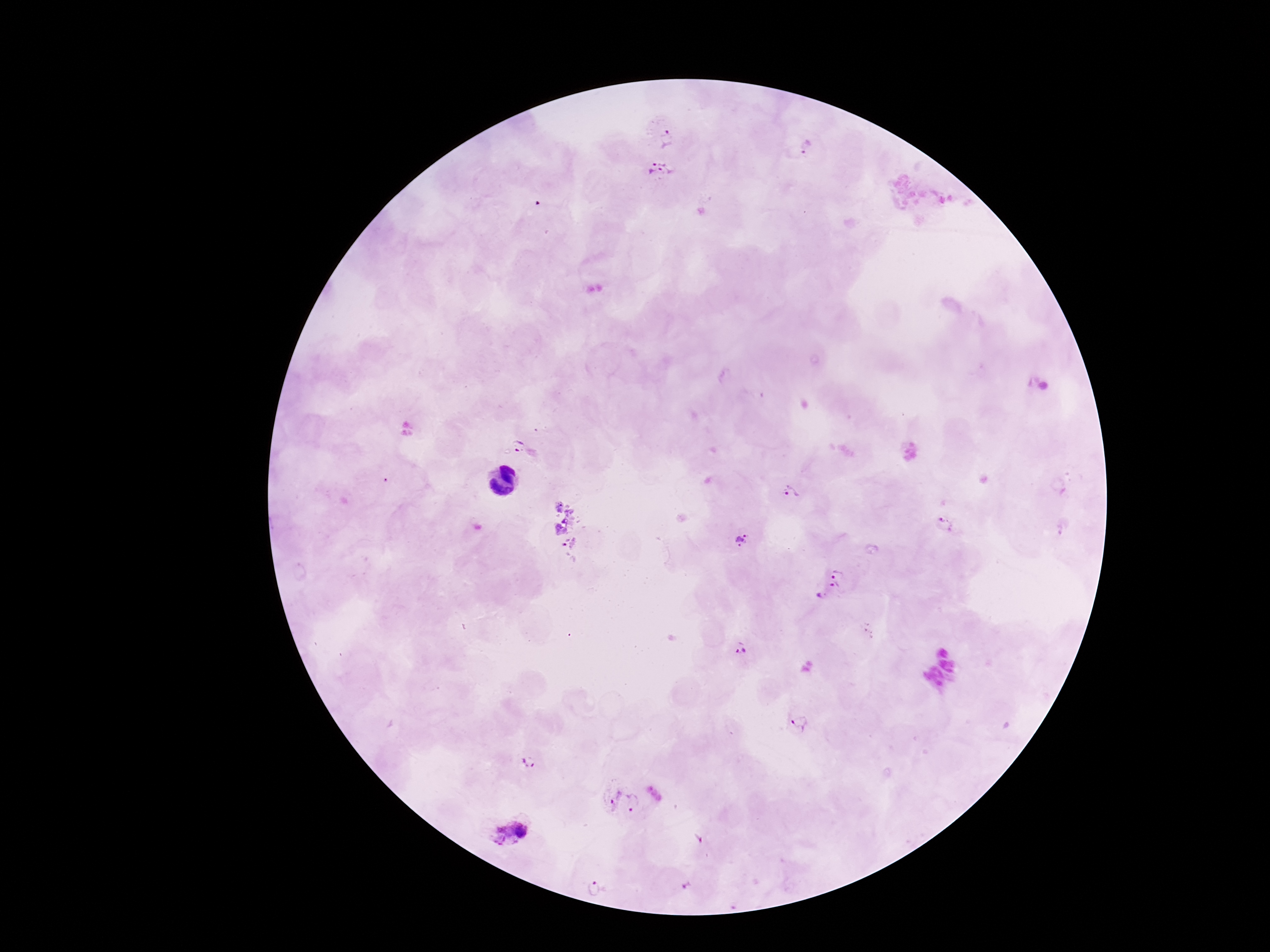
Approximate object centers, in pixels from the top-left corner. Plasmodium parasite locations: (x=667, y=136), (x=807, y=147), (x=659, y=173), (x=517, y=445), (x=791, y=492), (x=944, y=524), (x=742, y=541), (x=838, y=571), (x=828, y=592), (x=739, y=654), (x=800, y=722), (x=528, y=765), (x=623, y=802), (x=512, y=835), (x=595, y=888). Image is 1270×952 pixels. Giemsa-stained preparation. One field from this slide. Patient malaria status: positive. Photographed through the microscope eyepiece with a smartphone camera. 100x magnification. Thick blood smear.